Assess the morphology of the red blood cells.
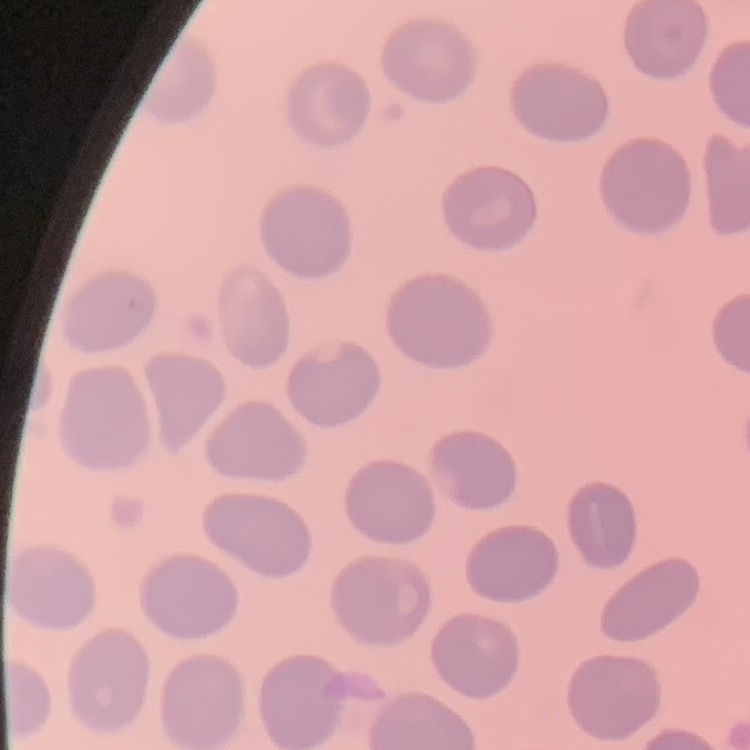

No rouleaux formation.

Field's or Giemsa stain. Thin blood smear. One tile cut from a larger photomicrograph.